Outline each blood parasite and name the species.
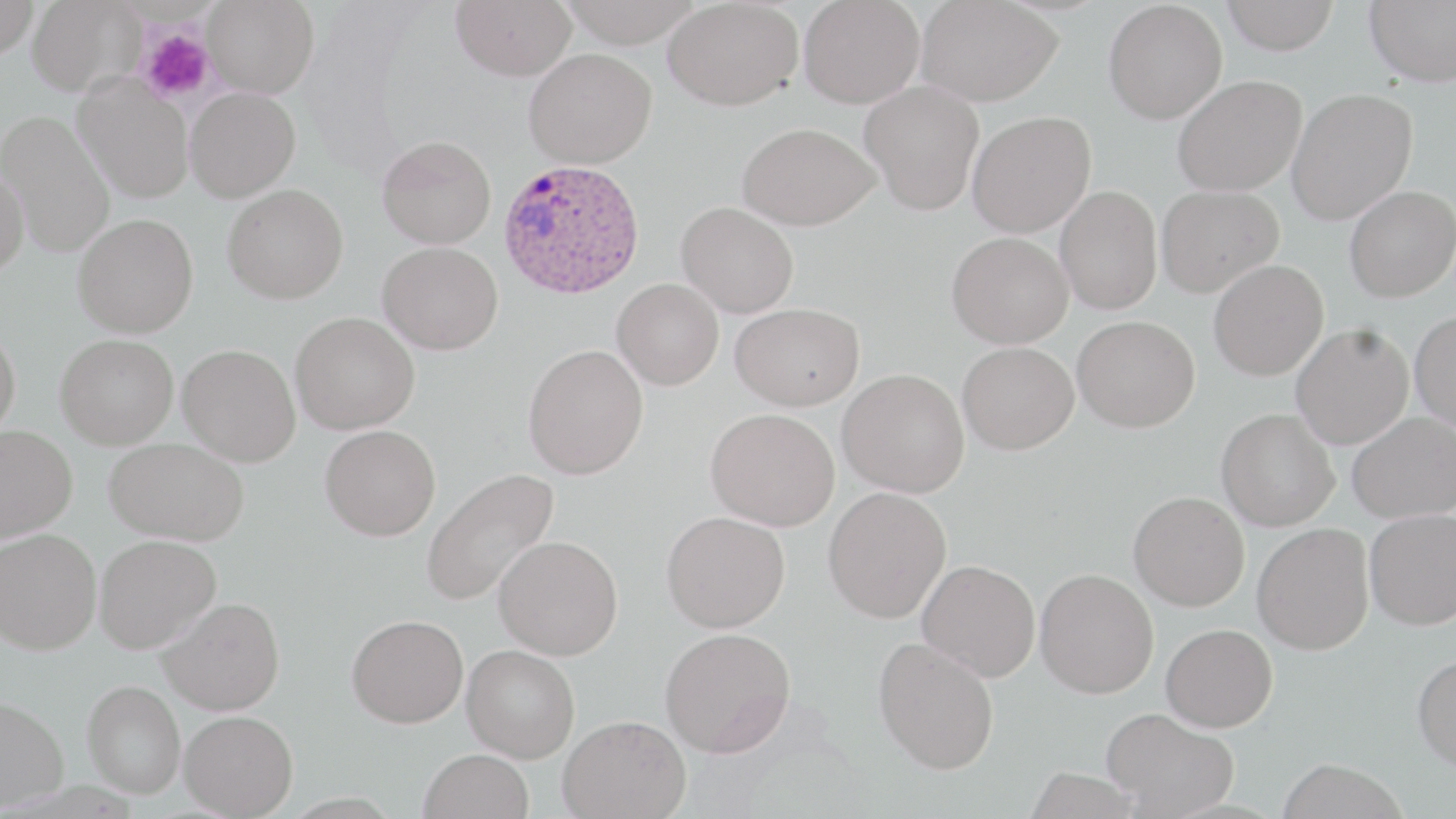

Approximate bounding boxes as [x1, y1, x2, y2] in pixels.
Plasmodium ovale-infected red blood cells: [497, 157, 646, 300].
No Plasmodium falciparum, Plasmodium malariae, Plasmodium vivax, Babesia divergens, or Trypanosoma brucei observed.

Platelet locations: [139, 29, 214, 103]. Uninfected red blood cell locations: [0, 0, 40, 59], [27, 0, 144, 97], [202, 0, 319, 98], [451, 0, 577, 81], [560, 0, 704, 47], [663, 0, 803, 111], [798, 0, 924, 108], [915, 0, 1062, 106], [1221, 0, 1339, 54], [1365, 0, 1456, 87], [1103, 1, 1228, 124], [524, 48, 657, 168], [73, 74, 194, 203], [1172, 75, 1307, 196], [859, 81, 984, 215], [185, 87, 300, 202], [1287, 87, 1418, 225], [1, 109, 116, 259], [967, 111, 1096, 237], [737, 122, 879, 230], [377, 135, 497, 249], [0, 165, 29, 278], [222, 184, 348, 304], [1156, 185, 1284, 297], [1344, 185, 1456, 302], [1055, 186, 1162, 315], [676, 202, 799, 318], [72, 213, 198, 338], [947, 232, 1073, 348], [378, 242, 503, 355], [1209, 260, 1328, 380], [612, 278, 724, 390], [730, 302, 864, 411], [1411, 310, 1456, 431], [290, 312, 419, 434], [1073, 315, 1200, 432], [1291, 324, 1413, 449], [0, 325, 21, 442], [55, 334, 178, 449], [957, 341, 1079, 454], [177, 344, 300, 467], [523, 344, 648, 479], [838, 368, 969, 497], [705, 408, 839, 531], [1216, 408, 1339, 531], [1348, 412, 1455, 523], [0, 425, 78, 541], [320, 425, 440, 541], [104, 437, 249, 545], [421, 467, 560, 607], [823, 486, 951, 623], [1128, 490, 1250, 610], [1365, 508, 1456, 630], [661, 510, 789, 632], [1252, 523, 1374, 654], [0, 528, 101, 654], [94, 534, 221, 654], [493, 535, 623, 659], [917, 559, 1040, 681], [1035, 569, 1159, 699], [158, 597, 285, 715], [346, 614, 468, 727], [1161, 623, 1278, 732], [660, 627, 796, 757], [873, 637, 1000, 774], [462, 644, 580, 762], [1412, 652, 1456, 773], [81, 680, 185, 798], [0, 695, 69, 812], [1101, 708, 1239, 817], [179, 710, 298, 818], [558, 715, 690, 819], [419, 749, 534, 819], [1276, 758, 1408, 819], [1023, 766, 1145, 818]. Slide-level diagnosis: Plasmodium ovale. Thin blood film. Captured at 1000x magnification. One field of a larger specimen. Optical microscopy. Image is 1456×819 pixels. May-Grünwald-Giemsa-stained preparation.